Assess this cell for malaria.
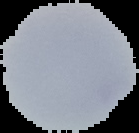
It is uninfected.

Image is 139×133 pixels. Cell region segmented out of the field of view; the surrounding area is masked to black. From a thin blood film.